Classify this cell by malaria status.
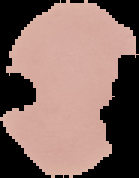
It is uninfected.

Summary:
  - Image size: 139×178 pixels
  - Preparation: thin blood smear
  - Image type: segmented cell region with the area outside set to black